State which cell type is depicted.
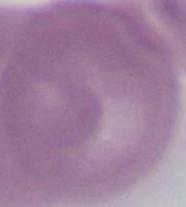
An erythrocyte.

magnification: 1000x
modality: photomicrograph